Assess this cell for malaria.
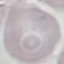
Uninfected.

Thin blood film. Cell patch, automatically extracted from a larger field of view and resized to 64 × 64 pixels. Acquired by smartphone through the microscope eyepiece. Giemsa stain.